Report the malaria status.
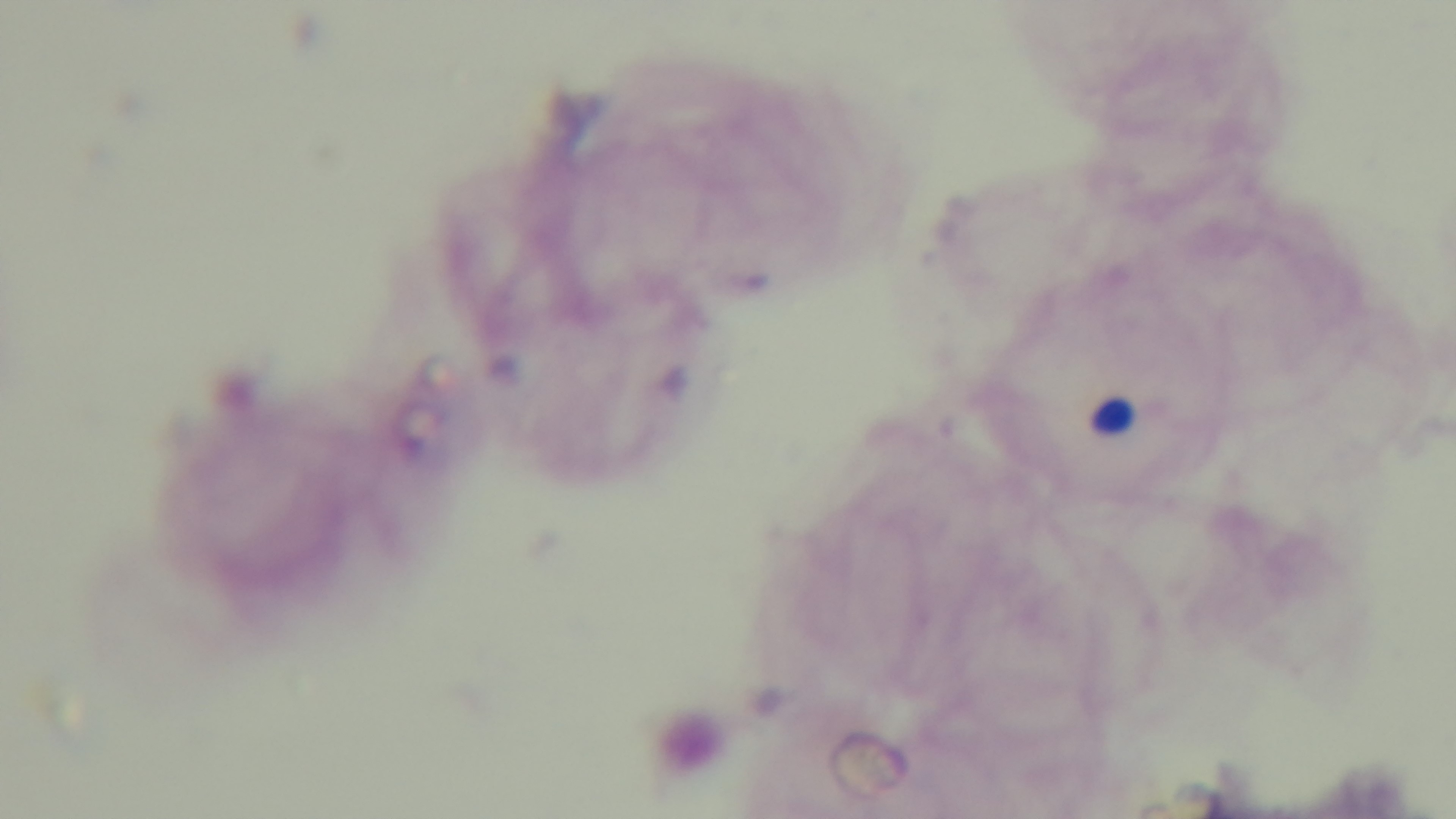

Negative.

{
  "objective": "100x oil immersion",
  "preparation": "thick",
  "field_of_view": "single",
  "stain": "Giemsa",
  "modality": "light microscopy",
  "capture": "mounted 4K digital camera"
}